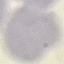
Result: no malaria parasites detected. Automatically extracted cell patch, resized to 64 × 64 pixels. Giemsa-stained preparation. Acquired by smartphone through the microscope eyepiece. Thin blood smear.